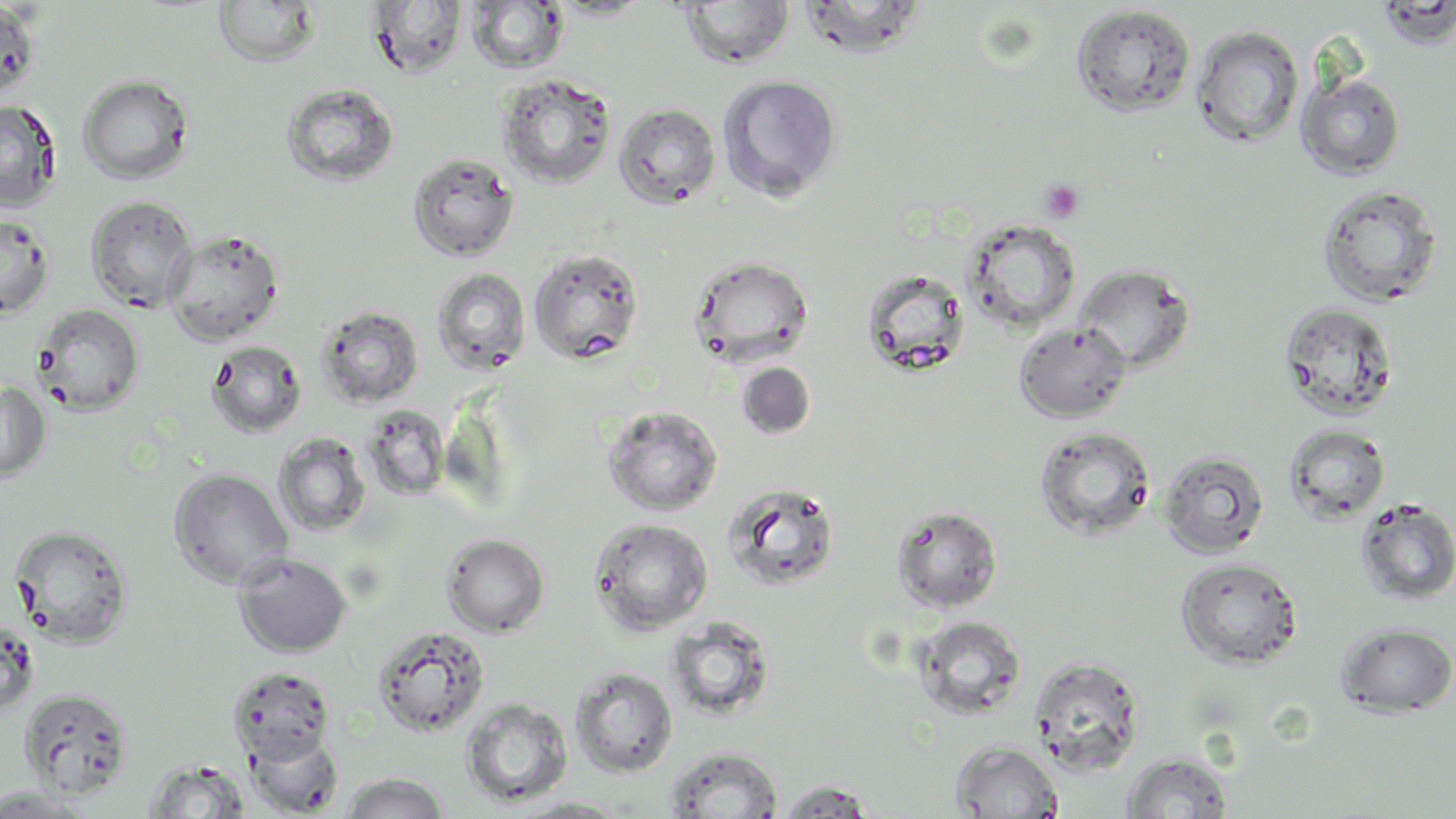
{
  "slide_level_diagnosis": "no evidence of blood parasites",
  "modality": "optical microscopy",
  "uninfected_red_blood_cell_locations": "approximate bounding boxes as (x1, y1, x2, y2) in pixels: (793, 0, 929, 58), (0, 1, 41, 102), (213, 1, 321, 68), (366, 1, 469, 79), (677, 1, 795, 69), (466, 2, 570, 75), (1070, 4, 1197, 118), (1190, 24, 1305, 147), (497, 72, 617, 188), (1296, 72, 1406, 180), (77, 74, 194, 184), (717, 74, 843, 202), (280, 83, 399, 187), (0, 100, 61, 212), (613, 103, 721, 209), (407, 153, 519, 262), (1316, 184, 1443, 308), (86, 195, 198, 312), (0, 212, 54, 319), (961, 218, 1082, 333), (165, 229, 284, 345), (528, 248, 644, 365), (688, 254, 815, 367), (1073, 264, 1196, 374), (431, 267, 531, 376), (860, 267, 971, 377), (1278, 302, 1400, 420), (32, 303, 145, 415), (316, 305, 424, 409), (1014, 321, 1132, 422), (206, 340, 307, 438), (737, 362, 816, 439), (0, 381, 51, 482), (602, 405, 723, 517), (361, 406, 452, 500), (1284, 424, 1390, 524), (1034, 426, 1156, 541), (272, 434, 371, 537), (1159, 450, 1270, 559), (168, 468, 293, 590), (720, 482, 842, 592), (1354, 497, 1456, 605), (891, 505, 1003, 613), (588, 518, 714, 635), (9, 524, 134, 647), (442, 534, 549, 636), (232, 552, 353, 657), (1176, 557, 1303, 669), (913, 615, 1027, 720), (666, 617, 774, 722), (0, 619, 39, 718), (1336, 622, 1455, 717), (372, 624, 490, 738), (1027, 656, 1146, 775), (228, 666, 335, 765), (570, 667, 678, 777), (19, 687, 133, 799), (460, 697, 574, 807), (246, 731, 343, 816), (950, 740, 1064, 818), (665, 746, 784, 818), (1121, 751, 1234, 818), (143, 759, 252, 818), (338, 772, 451, 818), (776, 780, 878, 816), (0, 786, 99, 817), (509, 797, 632, 818)",
  "magnification": "1000x",
  "preparation": "thin blood film",
  "platelet_locations": "approximate bounding boxes as (x1, y1, x2, y2) in pixels: (1039, 179, 1085, 223)",
  "field_of_view": "single",
  "image_size": "1456×819 pixels",
  "stain": "May-Grünwald-Giemsa"
}